State the blood parasite species.
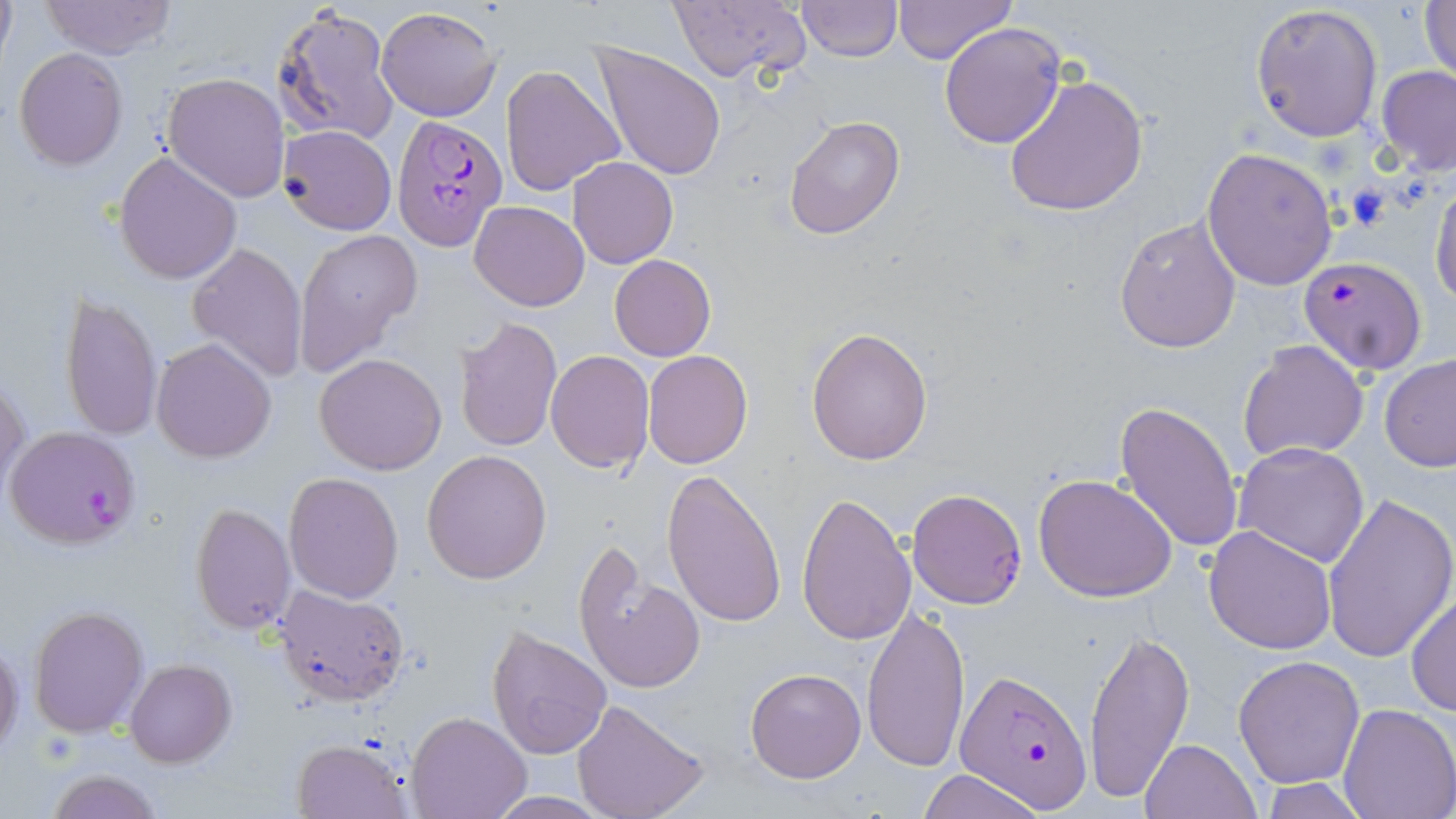

Plasmodium falciparum.

field_of_view: single
image_size: 1456×819 pixels
plasmodium_falciparum_infected_red_blood_cell_locations: 'approximate bounding boxes as (x1,y1)-(x2,y2) corner pairs in pixels: (391,115)-(506,251), (1300,256)-(1427,377), (3,425)-(141,551), (907,489)-(1029,610), (958,668)-(1094,814)'
modality: light microscopy
magnification: 1000x
stain: May-Grünwald-Giemsa
uninfected_red_blood_cell_locations: 'approximate bounding boxes as (x1,y1)-(x2,y2) corner pairs in pixels: (0,0)-(16,71), (667,0)-(812,84), (893,0)-(1017,67), (40,1)-(176,59), (797,1)-(900,63), (1421,1)-(1456,87), (271,3)-(399,146), (1250,3)-(1383,141), (376,6)-(502,122), (939,21)-(1067,149), (590,42)-(727,181), (13,47)-(128,170), (500,64)-(624,197), (1376,66)-(1456,176), (163,72)-(289,201), (1004,73)-(1150,216), (784,117)-(905,239), (279,124)-(397,235), (1202,146)-(1337,291), (114,150)-(243,285), (569,157)-(677,268), (1429,176)-(1456,305), (470,201)-(590,311), (1113,216)-(1240,354), (294,229)-(420,372), (187,242)-(309,381), (609,254)-(716,361), (61,291)-(163,442), (455,316)-(562,452), (806,325)-(933,467), (153,338)-(275,462), (1236,339)-(1369,462), (643,349)-(752,467), (546,350)-(654,473), (315,352)-(447,476), (1379,354)-(1456,473), (0,373)-(29,497), (1115,400)-(1242,554), (1232,441)-(1371,569), (421,449)-(551,584), (661,468)-(786,629), (283,473)-(404,603), (1033,473)-(1178,602), (797,491)-(915,646), (1321,492)-(1456,664), (189,502)-(296,634), (1204,524)-(1336,654), (573,544)-(705,698), (275,585)-(409,705), (1408,589)-(1455,718), (28,604)-(148,738), (862,607)-(969,774), (1083,623)-(1194,806), (486,625)-(614,761), (0,643)-(23,757), (1233,656)-(1365,788), (125,659)-(235,768), (745,667)-(866,784), (572,699)-(711,819), (1337,704)-(1456,819), (405,712)-(530,819), (291,737)-(411,818), (1140,738)-(1261,819), (47,769)-(163,819), (916,769)-(1047,819), (1256,778)-(1371,817), (482,792)-(614,817)'
preparation: thin blood smear